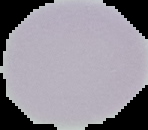 From a thin blood film. Image is 148×130 pixels. Malaria status: uninfected. Segmented cell region on a black background.